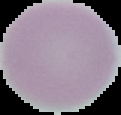

{
  "result": "negative for Plasmodium parasites",
  "image_size": "121×115 pixels",
  "image_type": "cell region segmented out of the field of view; surrounding area masked to black",
  "preparation": "thin blood smear"
}